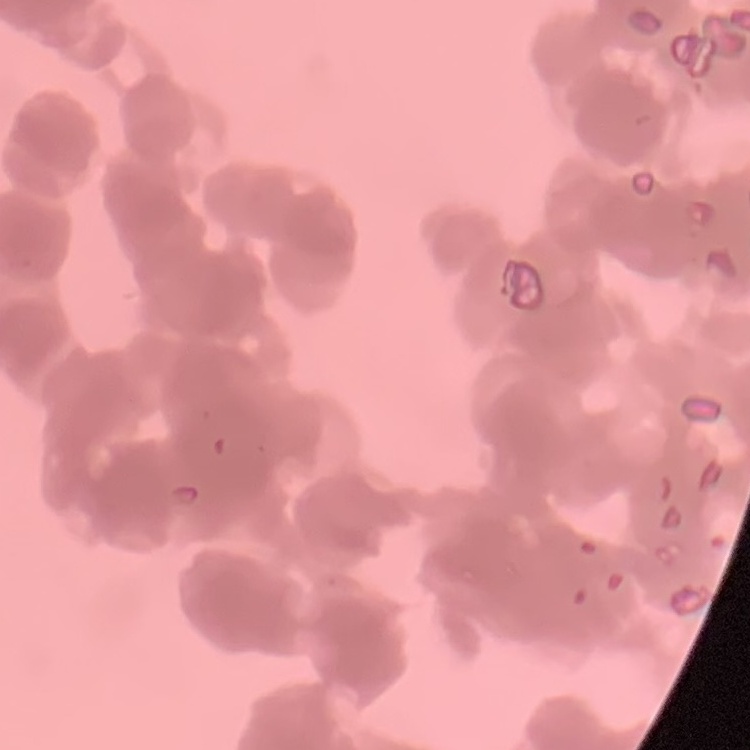

Summary:
  - Red blood cell morphology: rouleaux formation
  - Image type: square crop of a larger photomicrograph
  - Preparation: thin blood smear
  - Stain: Field's or Giemsa